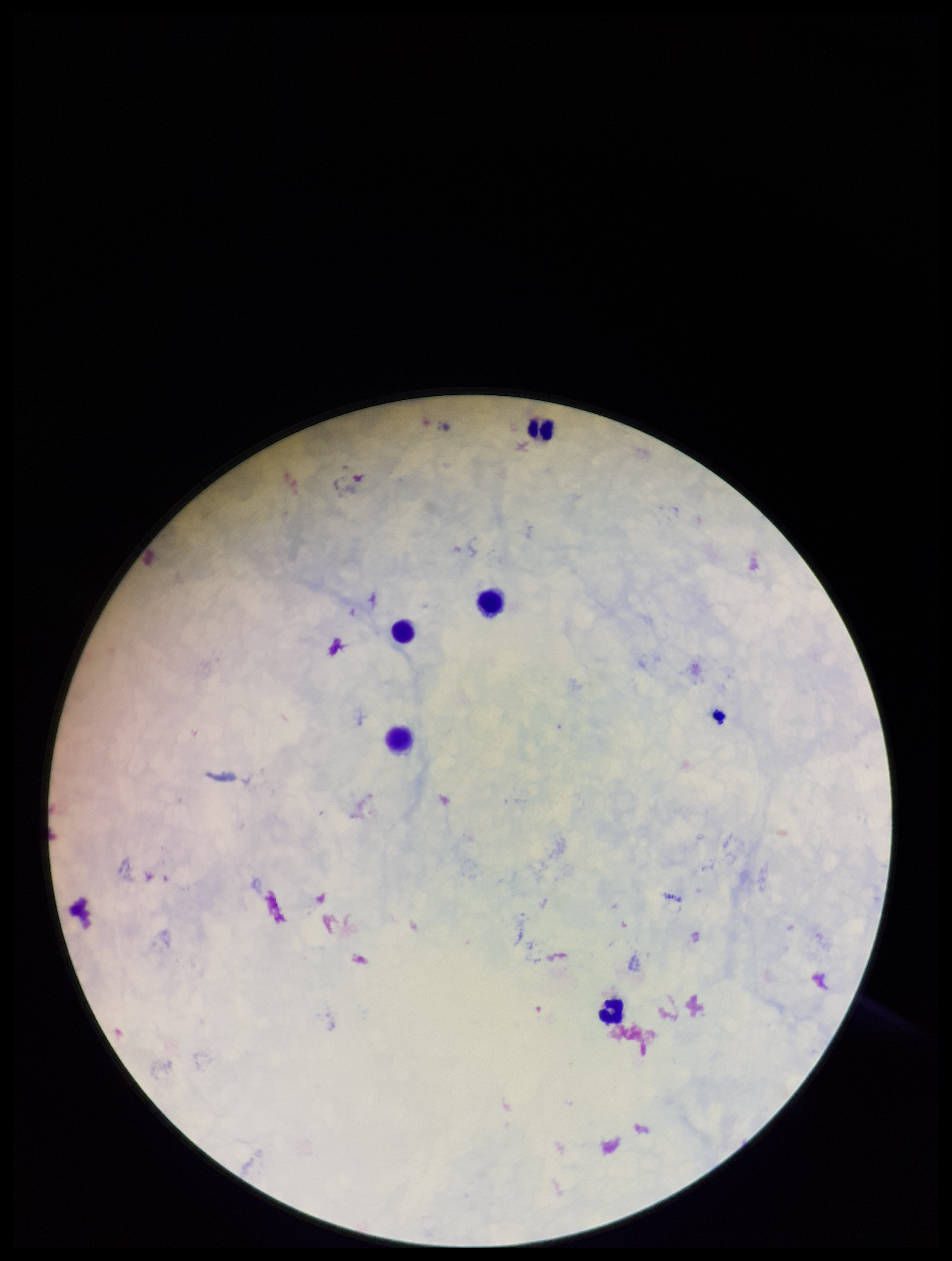 One field from this slide. Parasite count: 0. Leukocyte count: 5. Preparation: thick smear. Patient malaria status: negative. Photographed through the microscope eyepiece with a smartphone camera. Plasmodium parasites: none seen. Giemsa stain. Image is 952×1261 pixels.